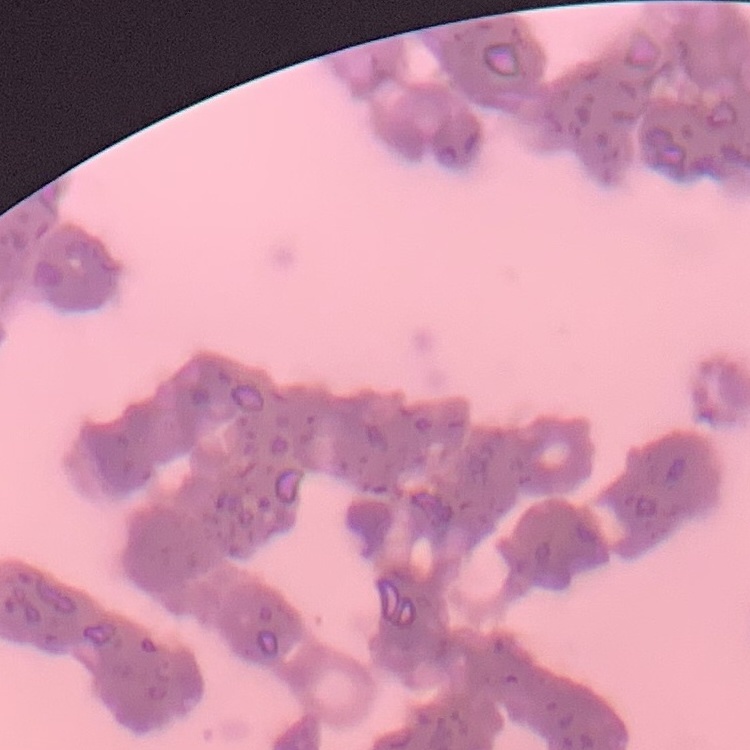

Summary:
  - Erythrocyte morphology: rouleaux formation
  - Stain: Field's or Giemsa
  - Image type: one tile cut from a larger photomicrograph
  - Preparation: thin blood smear